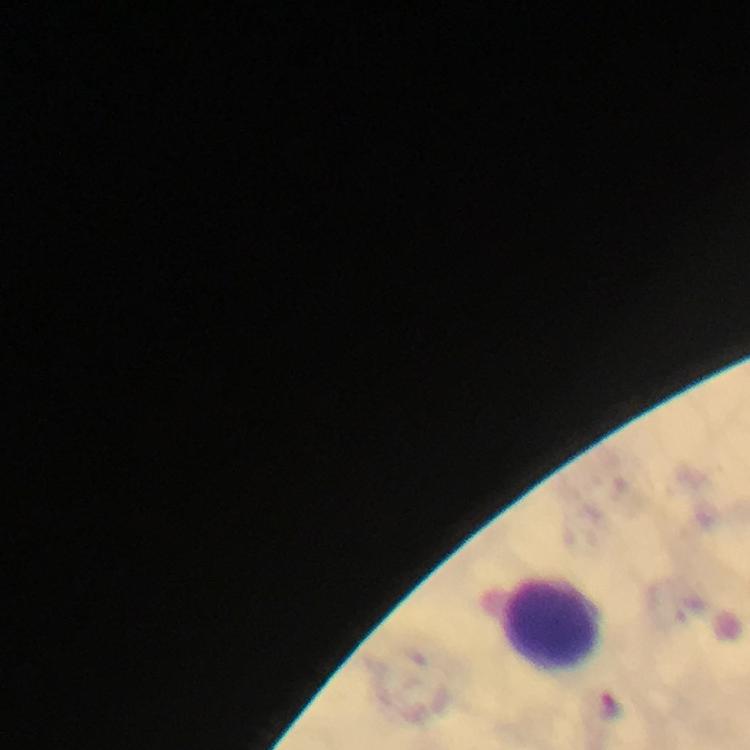 Approximate centers as (x, y) in pixels. Leukocyte locations: (551, 623). Photographed with a smartphone mounted on the microscope. A crop from one field of view. Malaria parasites: none seen. At 100x magnification. Thick blood film. Giemsa-stained preparation. From a malaria diagnostic workup. Image is 750×750 pixels. Immersion oil applied.